Identify the cell.
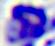

A leukocyte.

Micrograph. Captured at 400x magnification.